Report the malaria status of this cell.
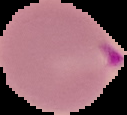

Parasitized.

The area outside the segmented cell region is set to black. Image is 127×115 pixels. From a thin blood smear.